Classify this cell by malaria status.
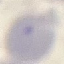
It is uninfected.

Thin blood film. Acquired by smartphone through the microscope eyepiece. Automatically extracted cell patch, resized to 64 × 64 pixels. Giemsa-stained preparation.